Point out each malaria parasite and each leukocyte.
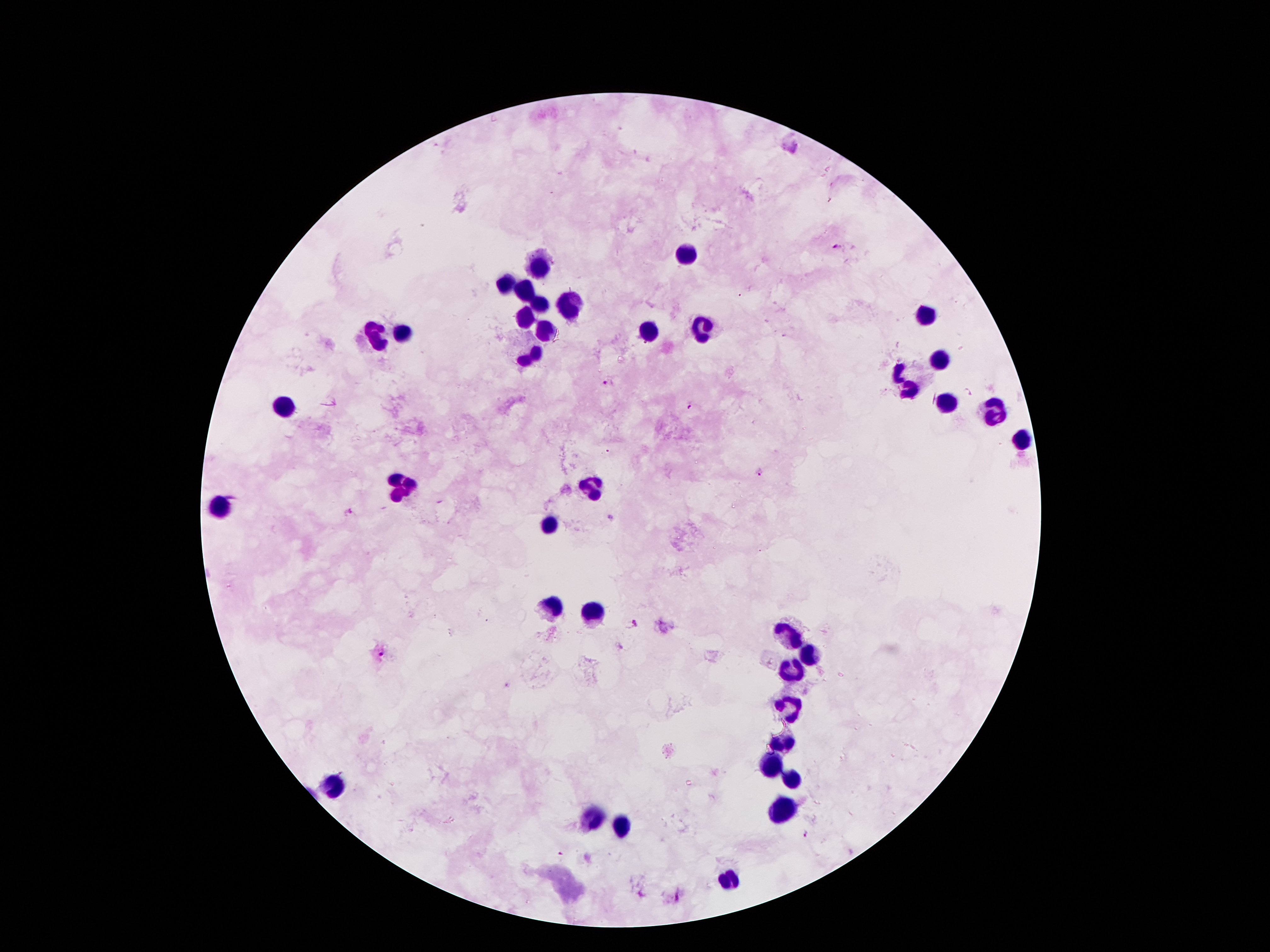
Approximate centers as [x, y] in pixels.
Malaria parasites: [837, 246], [607, 382], [968, 393], [691, 406], [760, 471], [348, 512], [610, 517], [632, 622], [380, 655], [805, 835], [560, 857].
Leukocytes: [686, 254], [537, 263], [506, 282], [522, 288], [539, 304], [571, 307], [926, 314], [526, 317], [702, 327], [545, 332], [650, 333], [398, 334], [374, 336], [532, 354], [940, 360], [899, 370], [912, 391], [945, 402], [283, 406], [997, 413], [1021, 436], [401, 487], [592, 487], [215, 505], [548, 525], [553, 606], [592, 614], [787, 636], [813, 656], [792, 672], [792, 709], [784, 743], [774, 767], [794, 777], [332, 786], [782, 804], [597, 820], [621, 829], [729, 877].

capture = smartphone camera through the microscope eyepiece
preparation = thick blood film
magnification = 100x
stain = Giemsa
image size = 1270×952 pixels
patient malaria status = positive for Plasmodium falciparum
field of view = single